Report the malaria status of this cell.
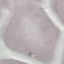

It is uninfected.

{
  "capture": "smartphone camera at the microscope eyepiece",
  "stain": "Giemsa",
  "image_type": "automatically extracted cell patch, resized to 64 × 64 pixels",
  "preparation": "thin smear"
}